Give the position of every Plasmodium parasite and every leukocyte.
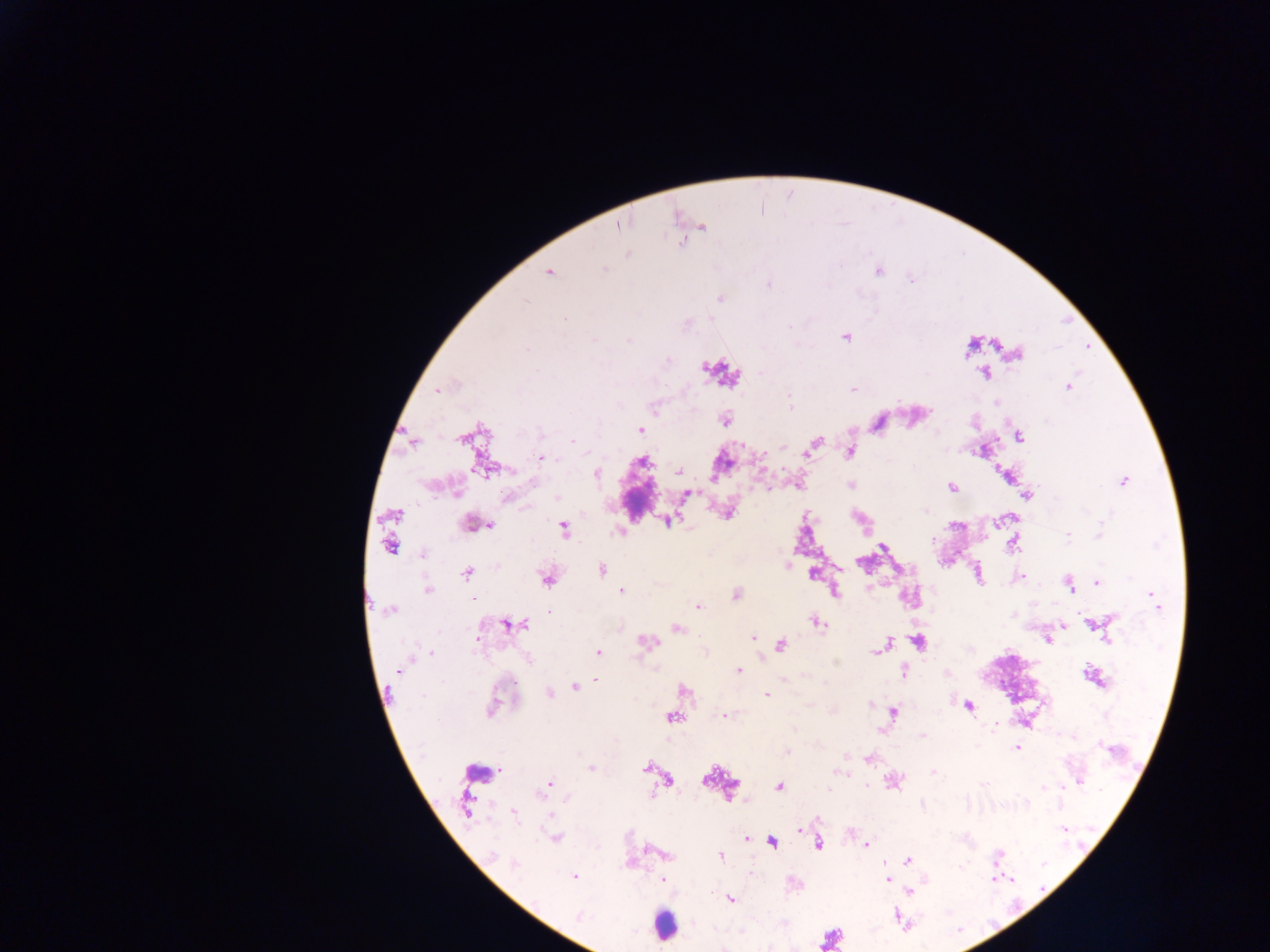
Approximate centers as x y in pixels.
Plasmodium parasites: 617 225; 700 228; 549 272; 845 336; 1088 346; 1015 353; 1067 386; 437 389; 853 389; 725 419; 639 430; 1019 436; 572 440; 815 442; 807 451; 850 451; 540 457; 596 473; 1007 475; 1123 480; 534 483; 797 484; 851 485; 952 486; 686 494; 1027 494; 728 512; 1000 520; 472 523; 488 525; 620 531; 1067 535; 1141 538; 1013 543; 423 554; 787 566; 841 568; 601 569; 813 573; 977 574; 1017 576; 1096 582; 1069 584; 427 590; 622 590; 833 591; 736 595; 470 598; 1153 600; 697 606; 390 610; 549 611; 817 622; 1093 622; 508 623; 1062 623; 676 628; 753 637; 1047 638; 1107 639; 646 642; 882 647; 598 653; 431 655; 400 669; 738 670; 903 672; 947 672; 1093 676; 596 677; 683 690; 549 693; 766 694; 967 705; 492 707; 724 715; 1016 747; 787 751; 869 758; 591 767; 651 767; 932 772; 891 781; 549 783; 779 786; 466 803; 513 812; 798 828; 555 837; 746 838; 866 844; 648 849; 665 854; 574 877; 663 879; 887 879; 1040 889; 897 915.
Leukocytes: 477 773; 663 924.

Sample from Ghana. Image is 1270×952 pixels. Photographed through a microscope with a mobile-phone camera. Single field of view. Thick blood film.